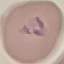

Summary:
  - Malaria status: parasitized
  - Capture: smartphone through the microscope eyepiece
  - Image type: automatically extracted cell patch, resized to 64 × 64 pixels
  - Preparation: thin smear
  - Stain: Giemsa